Identify the parasite.
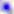
This is Toxoplasma gondii.

{
  "magnification": "400x",
  "modality": "photomicrograph"
}